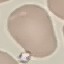 Result: no malaria parasites detected. Giemsa stain. Thin blood film. Photographed with a smartphone camera at the microscope eyepiece. Cell patch, automatically extracted from a larger field of view and resized to 64 × 64 pixels.